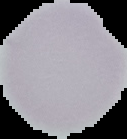
Summary:
  - Image type: segmented cell region on a black background
  - Preparation: thin blood film
  - Image size: 127×139 pixels
  - Malaria status: uninfected